Outline each Plasmodium ovale-infected red blood cell.
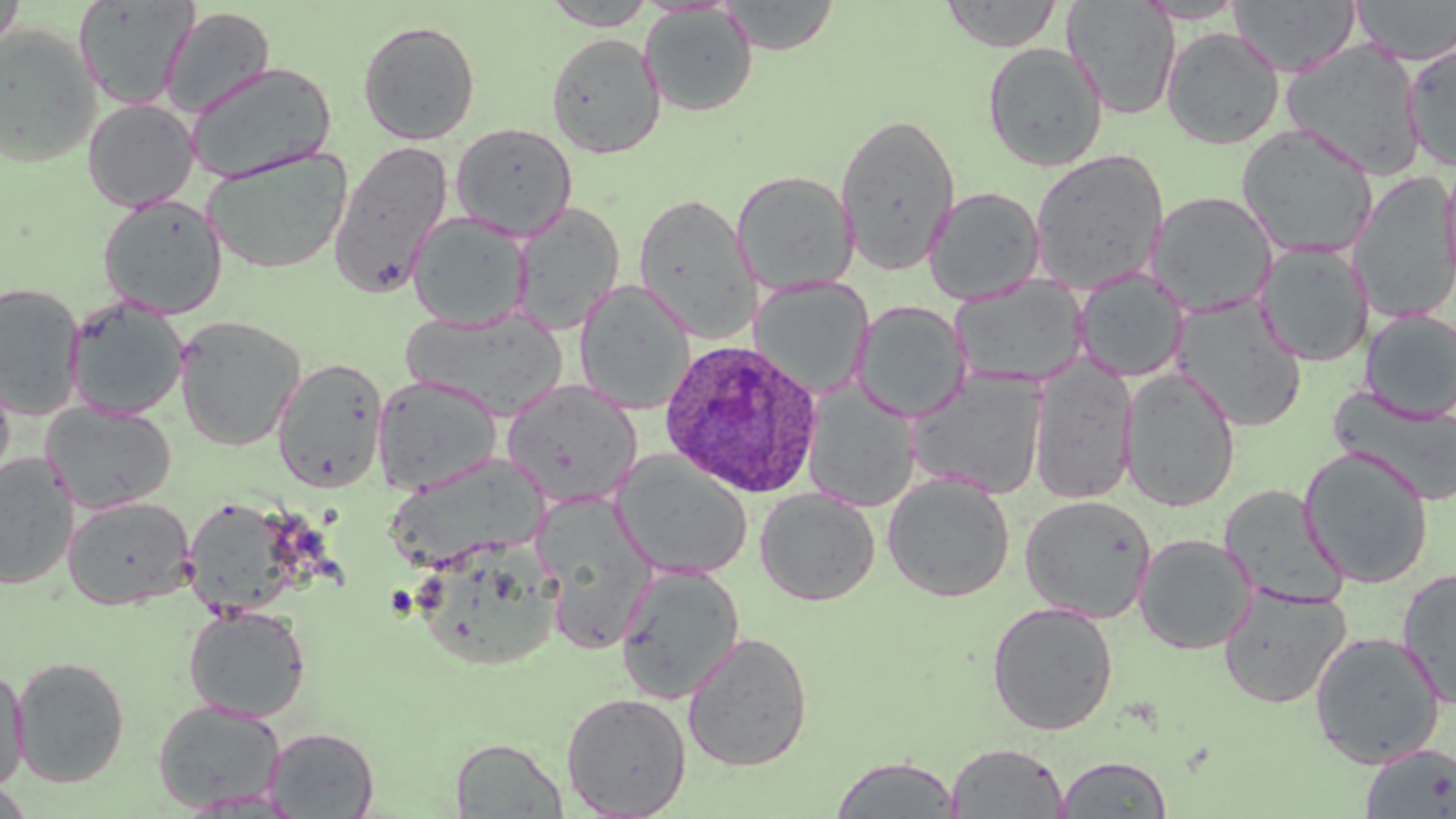
Approximate bounding boxes as (x1,y1)-(x2,y2) corner pairs in pixels.
Plasmodium ovale-infected red blood cells: (660,339)-(823,498).

Uninfected red blood cell locations: (0,0)-(26,54), (73,0)-(198,112), (542,0)-(656,29), (719,0)-(841,55), (940,0)-(1063,52), (1137,0)-(1247,23), (1230,0)-(1362,77), (1350,0)-(1456,65), (1062,1)-(1182,120), (640,4)-(758,116), (160,6)-(276,117), (358,20)-(480,145), (0,25)-(102,168), (1161,26)-(1285,149), (546,32)-(665,158), (1402,39)-(1456,171), (1282,40)-(1429,179), (982,42)-(1108,171), (185,61)-(337,183), (82,98)-(199,212), (836,112)-(960,276), (450,122)-(578,240), (1235,124)-(1380,259), (327,139)-(453,298), (202,148)-(354,275), (1030,148)-(1169,294), (1437,159)-(1456,298), (731,170)-(858,294), (1350,172)-(1456,324), (924,186)-(1046,305), (1147,191)-(1277,316), (632,193)-(761,342), (97,195)-(228,319), (511,202)-(625,334), (408,212)-(532,331), (1257,243)-(1373,367), (1074,270)-(1189,382), (951,276)-(1089,388), (750,278)-(873,398), (574,280)-(695,415), (0,281)-(85,419), (65,296)-(188,422), (1172,297)-(1308,432), (852,300)-(970,422), (400,308)-(569,420), (1359,310)-(1456,422), (174,315)-(306,451), (1028,355)-(1138,504), (272,358)-(388,493), (0,368)-(16,494), (1119,368)-(1240,512), (907,370)-(1049,499), (372,375)-(503,494), (502,379)-(643,508), (803,384)-(920,511), (1328,385)-(1456,508), (42,402)-(177,514), (1299,446)-(1434,588), (611,451)-(753,580), (0,452)-(80,590), (387,454)-(563,572), (882,473)-(1015,602), (1219,484)-(1347,608), (755,488)-(880,606), (532,493)-(659,652), (63,495)-(195,609), (1019,495)-(1157,624), (182,497)-(307,618), (1134,533)-(1256,654), (416,547)-(564,666), (614,564)-(746,703), (1396,566)-(1456,710), (1218,583)-(1351,709), (986,601)-(1119,736), (183,604)-(311,722), (1309,630)-(1446,768), (682,631)-(814,772), (11,655)-(130,787), (0,663)-(29,793), (561,692)-(692,818), (153,700)-(285,811), (264,727)-(379,817), (450,737)-(568,817), (945,742)-(1069,818), (1359,742)-(1456,818), (830,754)-(962,818), (1054,755)-(1172,818), (0,782)-(36,818). Slide-level diagnosis: Plasmodium ovale. Thin blood smear. May-Grünwald-Giemsa stain. Image is 1456×819 pixels. One field of a larger specimen. 1000x magnification. Optical microscopy.